Classify this cell by malaria status.
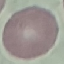

Uninfected.

{
  "stain": "Giemsa",
  "preparation": "thin blood film",
  "capture": "smartphone through the microscope eyepiece",
  "image_type": "cell patch, automatically extracted from a larger field of view and resized to 64 × 64 pixels"
}